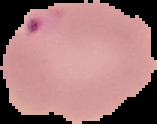
Summary:
  - Image size: 157×124 pixels
  - Image type: segmented cell region with the area outside set to black
  - Preparation: thin blood film
  - Malaria status: parasitized